Assess this cell for malaria.
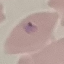

Parasitized.

preparation = thin blood film
capture = smartphone camera at the microscope eyepiece
image type = automatically extracted cell patch, resized to 64 × 64 pixels
stain = Giemsa